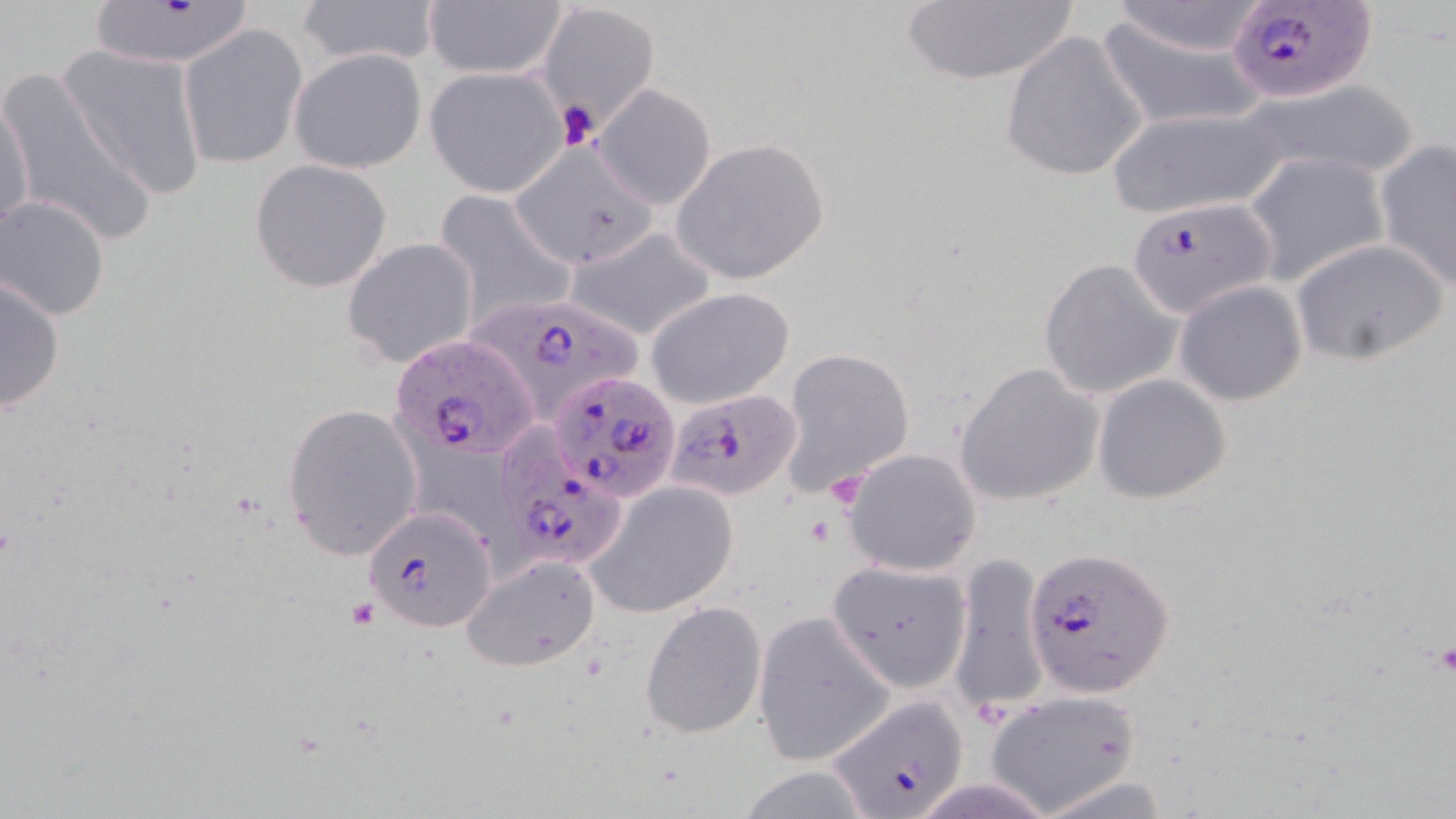
slide-level diagnosis = Plasmodium falciparum
field of view = single
stain = May-Grünwald-Giemsa
platelet locations = approximate bounding boxes as (x1, y1, x2, y2) in pixels: (556, 99, 600, 149)
uninfected red blood cell locations = approximate bounding boxes as (x1, y1, x2, y2) in pixels: (295, 0, 444, 68), (893, 0, 1085, 86), (424, 1, 568, 80), (1105, 1, 1272, 59), (538, 4, 657, 131), (1096, 15, 1269, 132), (179, 24, 307, 170), (999, 29, 1149, 184), (58, 46, 208, 199), (289, 48, 427, 174), (425, 67, 568, 197), (0, 68, 160, 251), (1241, 80, 1421, 182), (594, 83, 717, 209), (0, 93, 35, 240), (1105, 107, 1287, 221), (670, 138, 829, 284), (1376, 140, 1456, 290), (511, 142, 661, 270), (1244, 154, 1390, 286), (250, 158, 393, 293), (431, 187, 576, 323), (1, 196, 114, 321), (567, 228, 717, 342), (1289, 237, 1449, 366), (340, 238, 480, 369), (1037, 257, 1182, 400), (0, 273, 67, 416), (1173, 280, 1309, 406), (646, 287, 794, 409), (780, 347, 915, 492), (953, 361, 1103, 507), (1092, 374, 1232, 503), (283, 403, 424, 562), (840, 447, 982, 576), (585, 479, 738, 617), (950, 551, 1046, 716), (461, 554, 601, 671), (827, 558, 971, 690), (638, 599, 769, 740), (752, 612, 896, 768), (983, 689, 1143, 816)
magnification = 1000x
image size = 1456×819 pixels
preparation = thin blood film
Plasmodium falciparum-infected red blood cell locations = approximate bounding boxes as (x1, y1, x2, y2) in pixels: (85, 2, 256, 67), (1226, 2, 1376, 104), (1125, 195, 1274, 318), (461, 291, 645, 424), (388, 335, 536, 462), (550, 369, 682, 502), (663, 384, 802, 504), (496, 438, 630, 576), (362, 507, 497, 633), (1025, 544, 1173, 696), (825, 695, 970, 817)
modality = light microscopy